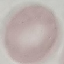 Malaria status: uninfected. Photographed with a smartphone camera at the microscope eyepiece. Giemsa stain. Thin blood film. Automatically extracted cell patch, resized to 64 × 64 pixels.